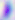
Summary:
  - Identification: Toxoplasma gondii
  - Magnification: 400x
  - Modality: photomicrograph